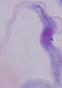

Captured at 1000x magnification. A trypanosome is shown. Micrograph.